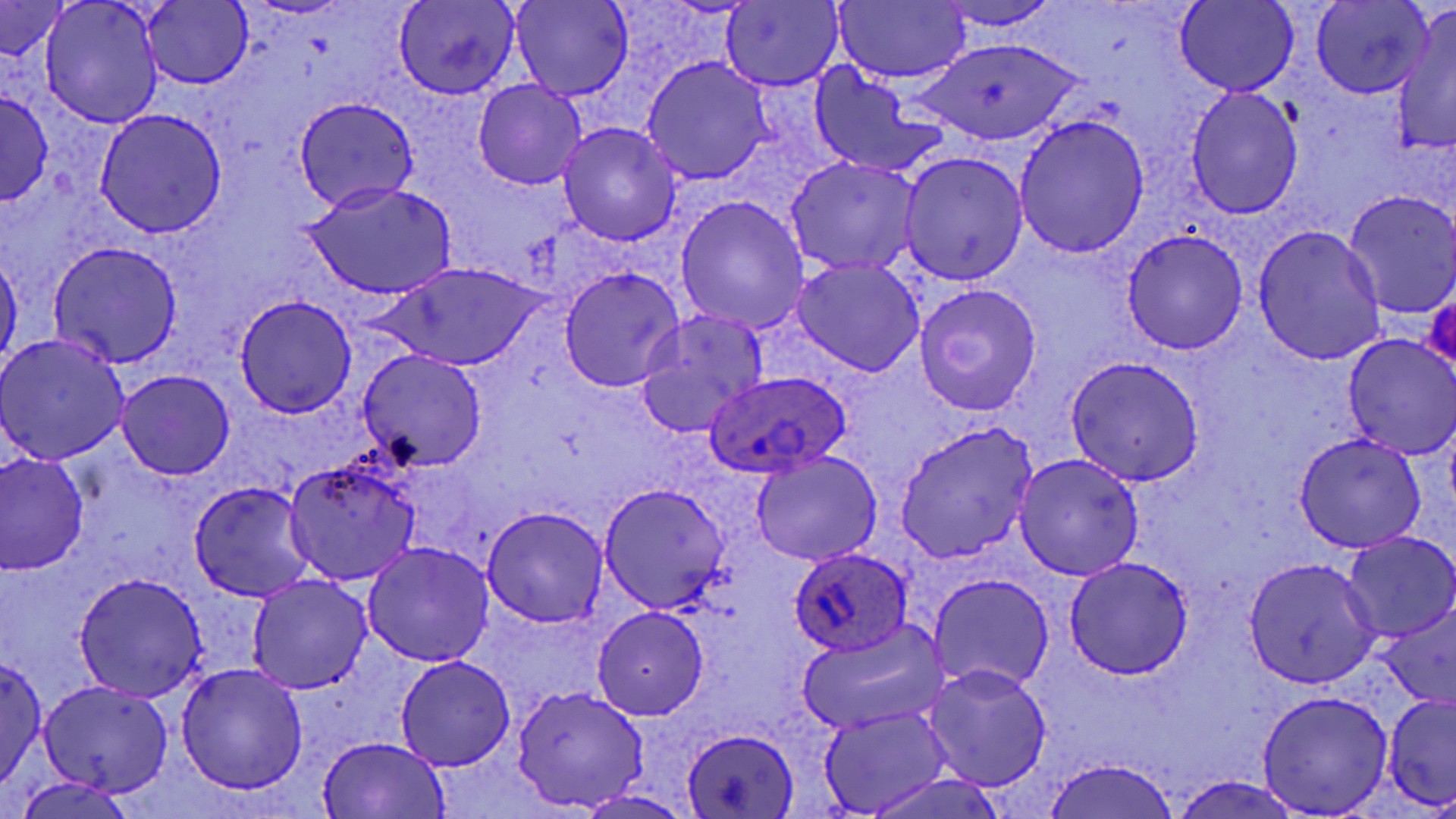

Approximate bounding boxes as named x1/y1/x2/y2 corners in pixels. Uninfected red blood cell locations: (x1=40, y1=0, x2=163, y2=126), (x1=835, y1=0, x2=970, y2=83), (x1=933, y1=1, x2=1064, y2=32), (x1=1175, y1=1, x2=1298, y2=97), (x1=143, y1=2, x2=253, y2=88), (x1=393, y1=2, x2=520, y2=100), (x1=510, y1=2, x2=634, y2=102), (x1=722, y1=2, x2=844, y2=90), (x1=1311, y1=2, x2=1433, y2=97), (x1=0, y1=3, x2=72, y2=59), (x1=1389, y1=14, x2=1456, y2=159), (x1=913, y1=38, x2=1086, y2=147), (x1=642, y1=57, x2=774, y2=185), (x1=809, y1=65, x2=947, y2=178), (x1=472, y1=78, x2=588, y2=191), (x1=1186, y1=87, x2=1304, y2=219), (x1=1, y1=89, x2=53, y2=204), (x1=293, y1=96, x2=420, y2=212), (x1=94, y1=109, x2=228, y2=238), (x1=1013, y1=115, x2=1150, y2=259), (x1=559, y1=122, x2=682, y2=245), (x1=899, y1=151, x2=1028, y2=284), (x1=785, y1=156, x2=920, y2=275), (x1=305, y1=181, x2=457, y2=299), (x1=1342, y1=190, x2=1456, y2=319), (x1=675, y1=196, x2=809, y2=335), (x1=1252, y1=225, x2=1387, y2=365), (x1=1122, y1=228, x2=1249, y2=354), (x1=49, y1=241, x2=183, y2=369), (x1=0, y1=254, x2=21, y2=371), (x1=793, y1=257, x2=924, y2=377), (x1=381, y1=263, x2=548, y2=370), (x1=560, y1=266, x2=684, y2=392), (x1=916, y1=284, x2=1042, y2=414), (x1=234, y1=295, x2=357, y2=417), (x1=634, y1=310, x2=770, y2=437), (x1=0, y1=333, x2=130, y2=465), (x1=1343, y1=335, x2=1455, y2=458), (x1=358, y1=349, x2=488, y2=472), (x1=1065, y1=356, x2=1205, y2=484), (x1=115, y1=368, x2=236, y2=480), (x1=895, y1=421, x2=1040, y2=562), (x1=1293, y1=433, x2=1426, y2=552), (x1=0, y1=451, x2=89, y2=575), (x1=749, y1=451, x2=884, y2=567), (x1=1013, y1=453, x2=1144, y2=580), (x1=284, y1=458, x2=421, y2=586), (x1=190, y1=481, x2=317, y2=601), (x1=599, y1=484, x2=729, y2=609), (x1=481, y1=507, x2=608, y2=628), (x1=1342, y1=532, x2=1456, y2=641), (x1=363, y1=541, x2=493, y2=666), (x1=1065, y1=556, x2=1194, y2=678), (x1=1245, y1=557, x2=1381, y2=687), (x1=73, y1=574, x2=206, y2=702), (x1=247, y1=575, x2=372, y2=693), (x1=930, y1=576, x2=1053, y2=691), (x1=1376, y1=605, x2=1454, y2=710), (x1=592, y1=607, x2=710, y2=720), (x1=798, y1=619, x2=952, y2=735), (x1=0, y1=655, x2=46, y2=796), (x1=394, y1=656, x2=517, y2=772), (x1=176, y1=662, x2=308, y2=794), (x1=920, y1=664, x2=1053, y2=789), (x1=39, y1=679, x2=174, y2=796), (x1=512, y1=686, x2=646, y2=812), (x1=1256, y1=690, x2=1393, y2=816), (x1=1383, y1=693, x2=1456, y2=810), (x1=817, y1=707, x2=953, y2=815), (x1=682, y1=728, x2=800, y2=817), (x1=318, y1=736, x2=450, y2=817), (x1=1042, y1=757, x2=1182, y2=819), (x1=862, y1=769, x2=1007, y2=819), (x1=1170, y1=775, x2=1305, y2=818), (x1=14, y1=776, x2=135, y2=819), (x1=576, y1=790, x2=695, y2=819). Plasmodium ovale-infected red blood cell locations: (x1=705, y1=370, x2=851, y2=477), (x1=789, y1=546, x2=913, y2=657). Slide-level diagnosis: Plasmodium ovale. Light microscopy. Thin blood film. Captured at 1000x magnification. May-Grünwald-Giemsa-stained preparation. Image is 1456×819 pixels. One field of a larger specimen.